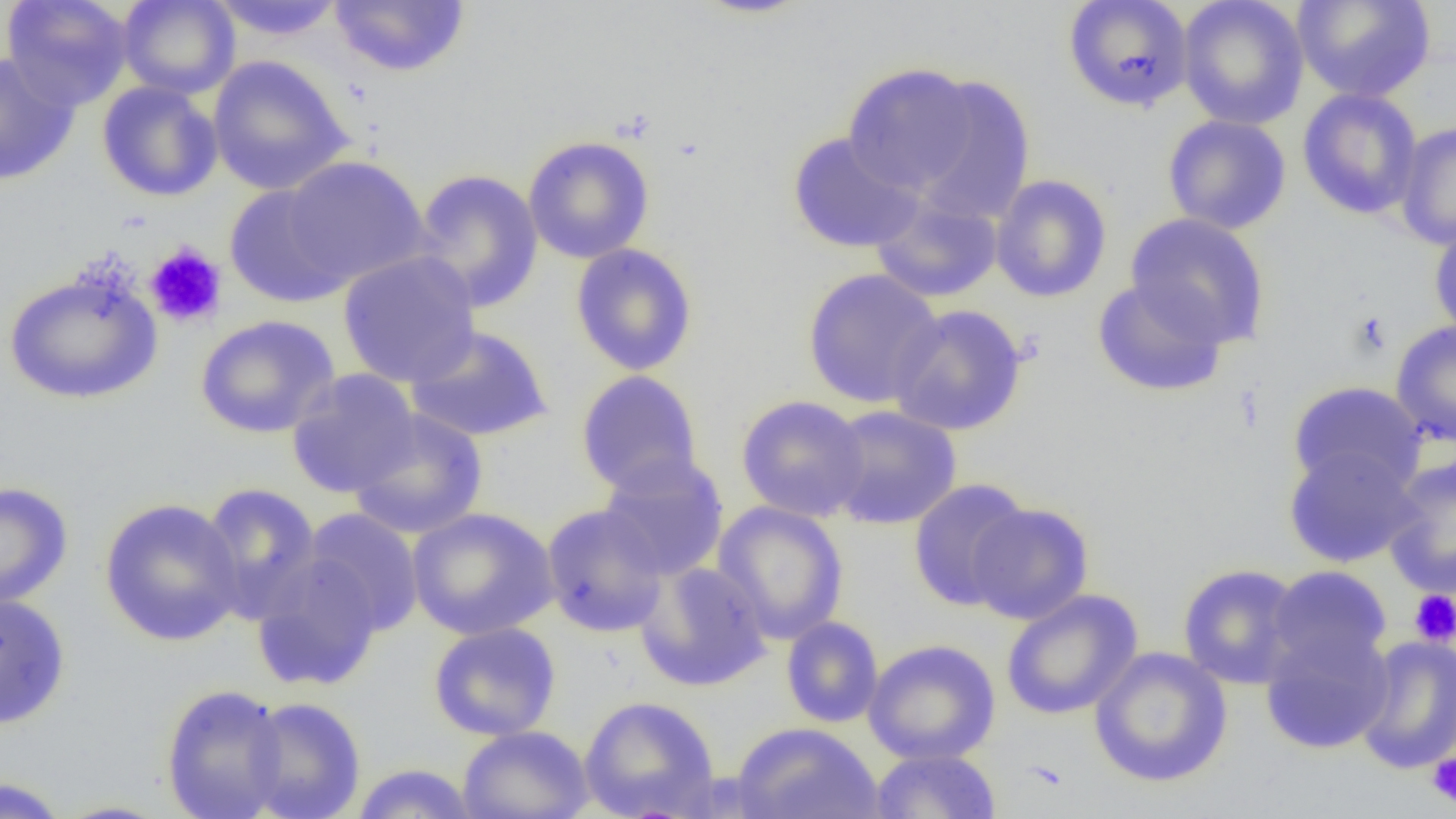

slide_level_diagnosis: negative for blood parasites
uninfected_red_blood_cell_locations: 'approximate bounding boxes as (x1, y1, x2, y2) in pixels: (1, 0, 134, 110), (117, 0, 240, 99), (208, 0, 346, 41), (691, 0, 814, 19), (1063, 0, 1194, 112), (1177, 0, 1309, 129), (1293, 0, 1435, 102), (328, 1, 471, 77), (0, 51, 81, 186), (207, 54, 353, 196), (841, 62, 980, 195), (906, 73, 1037, 224), (97, 81, 223, 202), (1297, 87, 1423, 220), (1162, 114, 1292, 234), (1394, 121, 1456, 250), (786, 131, 925, 254), (522, 135, 655, 264), (281, 156, 430, 287), (411, 168, 544, 313), (990, 174, 1112, 303), (224, 185, 353, 308), (869, 193, 1003, 304), (1125, 213, 1271, 349), (1429, 219, 1456, 339), (570, 243, 699, 376), (337, 251, 481, 388), (2, 265, 164, 405), (802, 268, 944, 409), (1091, 278, 1228, 398), (887, 303, 1028, 436), (194, 314, 340, 439), (1390, 320, 1456, 447), (405, 324, 553, 444), (285, 369, 421, 498), (575, 370, 704, 498), (1288, 381, 1426, 495), (735, 394, 870, 522), (824, 405, 962, 530), (347, 408, 489, 539), (1283, 446, 1421, 568), (597, 454, 729, 582), (1382, 456, 1456, 600), (907, 478, 1033, 611), (0, 481, 74, 612), (198, 482, 323, 622), (99, 497, 245, 647), (712, 501, 850, 645), (966, 502, 1095, 625), (540, 504, 669, 637), (407, 507, 559, 641), (301, 508, 425, 636), (251, 554, 384, 693), (634, 560, 772, 692), (1177, 563, 1306, 689), (1265, 565, 1393, 680), (1001, 589, 1143, 720), (0, 593, 71, 730), (780, 616, 884, 728), (428, 621, 562, 741), (1259, 627, 1395, 755), (1354, 634, 1456, 774), (863, 638, 1001, 766), (1088, 647, 1233, 788), (160, 683, 289, 819), (579, 695, 720, 819), (242, 697, 365, 819), (730, 722, 884, 819), (457, 725, 594, 819), (870, 748, 1001, 819), (349, 763, 481, 818), (0, 775, 71, 818), (50, 799, 176, 818)'
preparation: thin blood film
platelet_locations: 'approximate bounding boxes as (x1, y1, x2, y2) in pixels: (144, 243, 227, 329), (1350, 311, 1392, 358), (1409, 589, 1456, 646), (1426, 752, 1456, 808)'
image_size: 1456×819 pixels
magnification: 1000x
modality: optical microscopy
field_of_view: one of a larger specimen